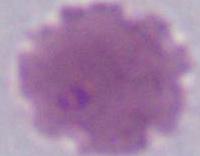
Summary:
  - Identification: erythrocyte
  - Modality: micrograph
  - Magnification: 1000x